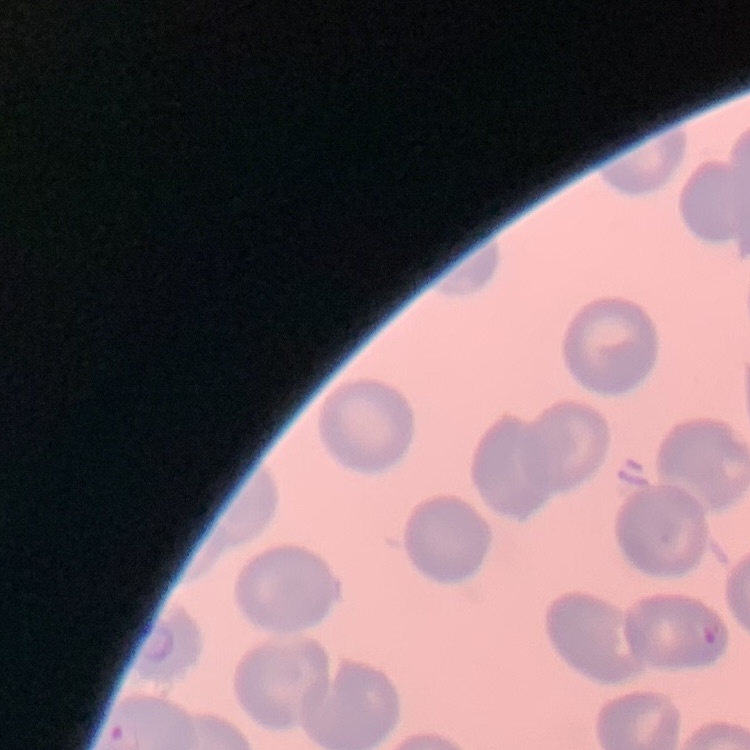

erythrocyte morphology = no rouleaux formation
stain = Field's or Giemsa
image type = square crop of a larger photomicrograph
preparation = thin peripheral smear